Evaluate for malaria.
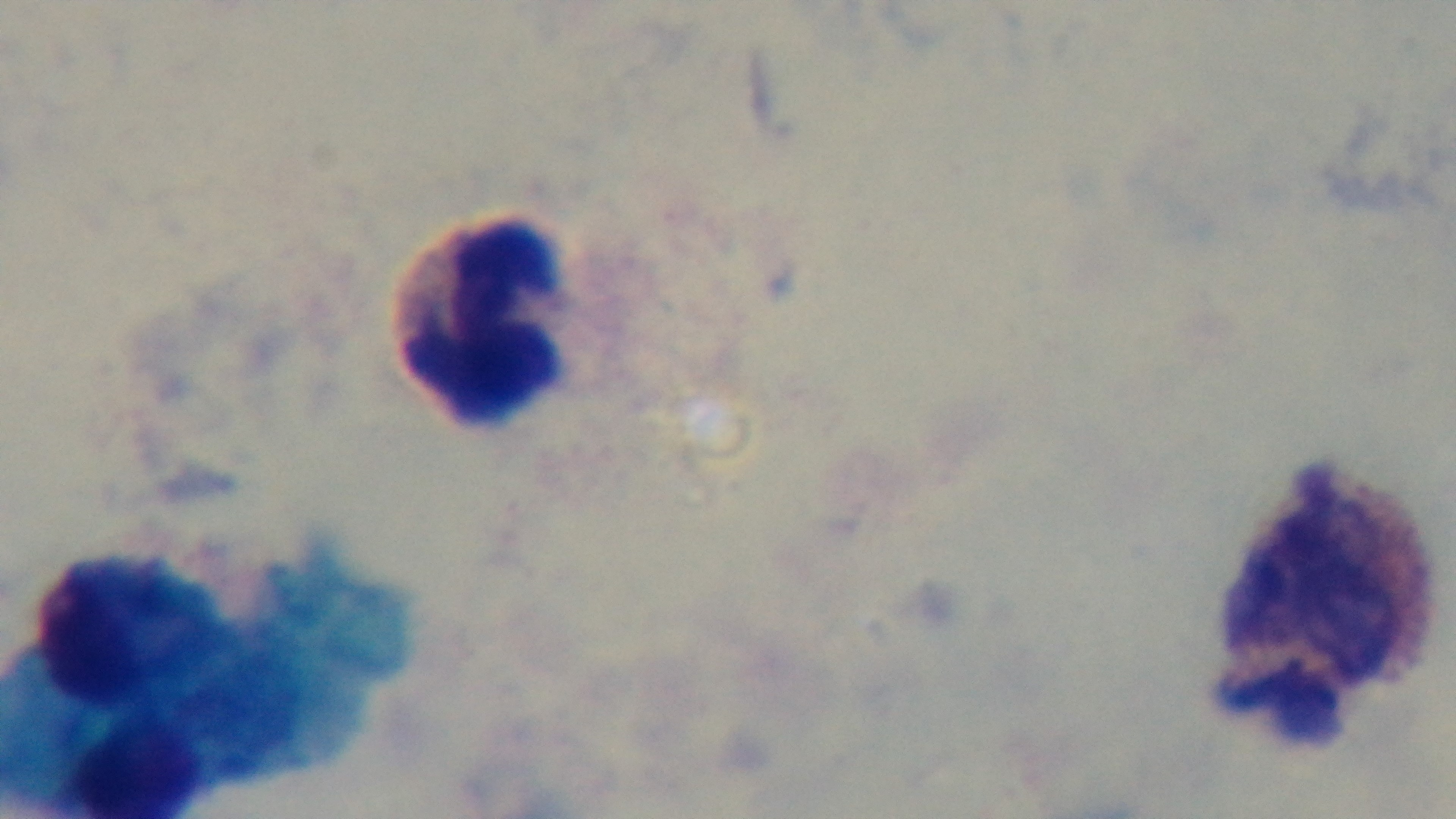

Uninfected.

Summary:
  - Capture: mounted 4K digital camera
  - Stain: Giemsa
  - Field of view: one from the slide
  - Preparation: thick blood film
  - Objective: 100x oil immersion
  - Modality: light microscopy